Classify this cell by malaria status.
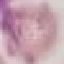
Uninfected.

Giemsa stain. Cell patch, automatically extracted from a larger field of view and resized to 64 × 64 pixels. Acquired by smartphone through the microscope eyepiece. Thin smear of blood.